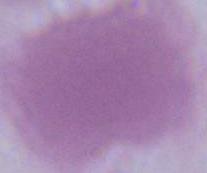

identification = red blood cell
magnification = 1000x
modality = photomicrograph